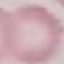

result = no malaria parasites seen
image type = cell patch, automatically extracted from a larger field of view and resized to 64 × 64 pixels
capture = smartphone camera at the microscope eyepiece
stain = Giemsa
preparation = thin blood smear